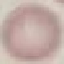

Result: no malaria parasites detected. Thin smear of blood. Cell patch, automatically extracted from a larger field of view and resized to 64 × 64 pixels. Acquired by smartphone through the microscope eyepiece. Giemsa stain.